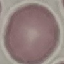

result = negative for malaria parasites
stain = Giemsa
capture = smartphone camera at the microscope eyepiece
image type = automatically extracted cell patch, resized to 64 × 64 pixels
preparation = thin blood smear